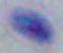

Summary:
  - Modality: micrograph
  - Magnification: 1000x
  - Identification: Toxoplasma gondii